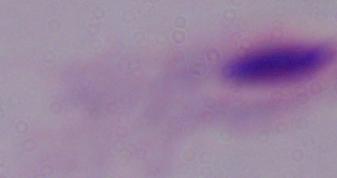 Micrograph. Captured at 1000x magnification. A trichomonad is seen.